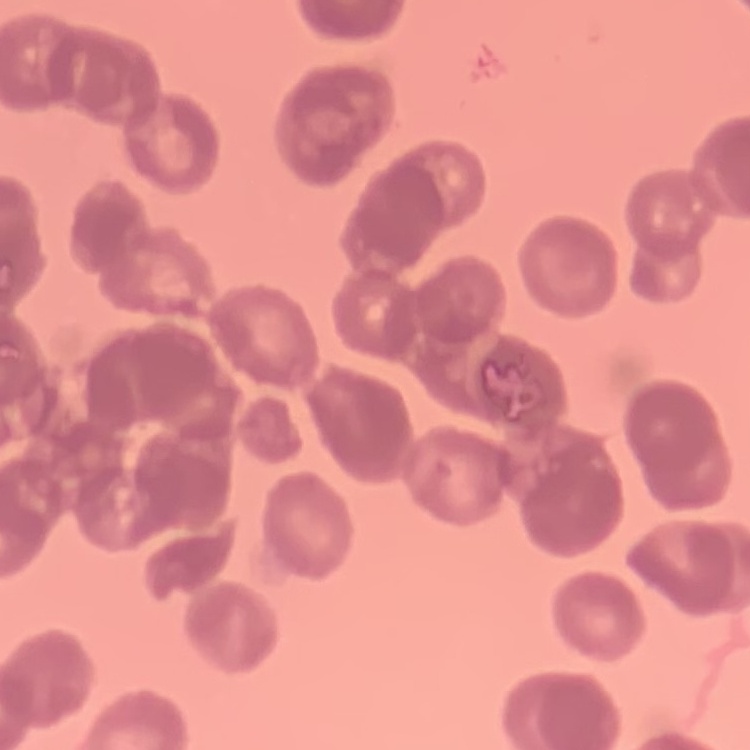
{
  "red_blood_cell_morphology": "rouleaux formation",
  "stain": "Field's or Giemsa",
  "image_type": "one tile cut from a larger photomicrograph",
  "preparation": "thin blood film"
}